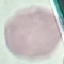
Malaria status: uninfected. Cell patch, automatically extracted from a larger field of view and resized to 64 × 64 pixels. Acquired by smartphone through the microscope eyepiece. Thin blood smear. Giemsa-stained preparation.